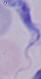
Summary:
  - Identification: trypanosome
  - Modality: micrograph
  - Magnification: 1000x